Identify the parasite.
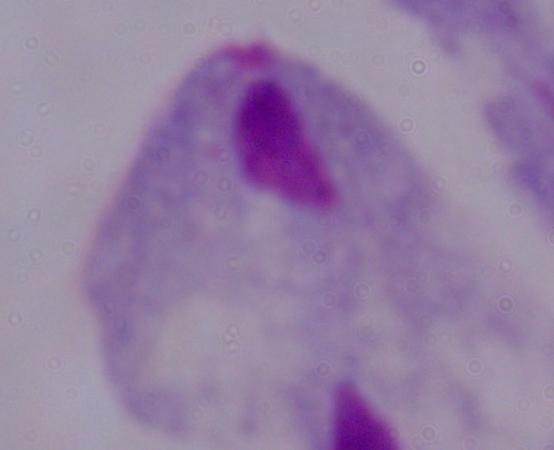
This is a trichomonad.

Captured at 1000x magnification. Photomicrograph.